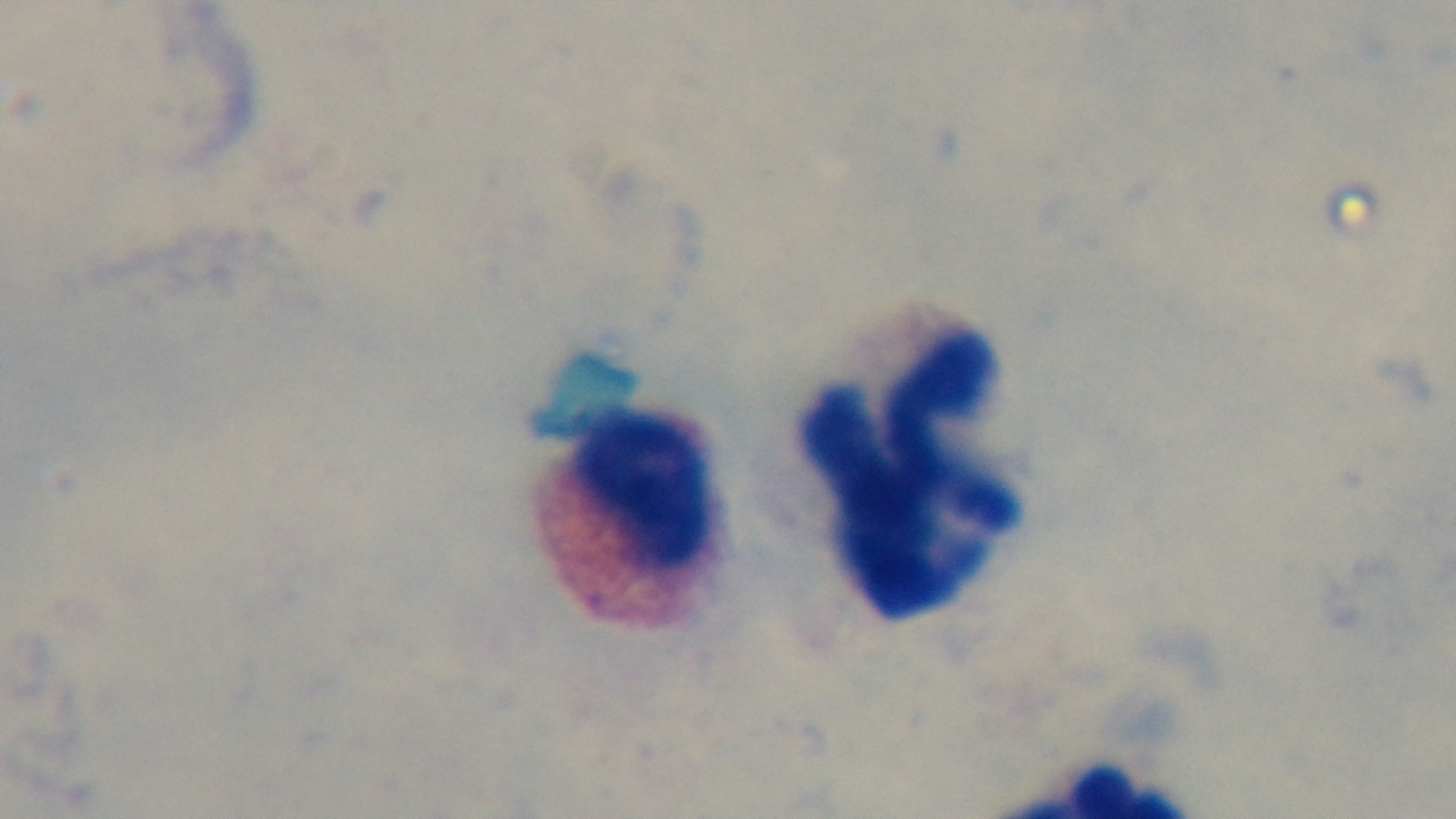

malaria status = uninfected
field of view = single
modality = light microscopy
objective = 100x oil immersion
stain = Giemsa
capture = mounted 4K digital camera
preparation = thick blood film